State which parasite is depicted.
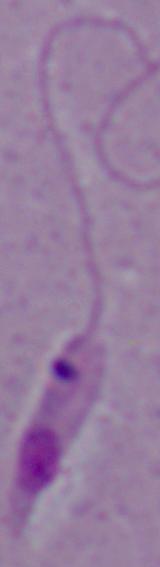

Leishmania.

Micrograph. 1000x magnification.